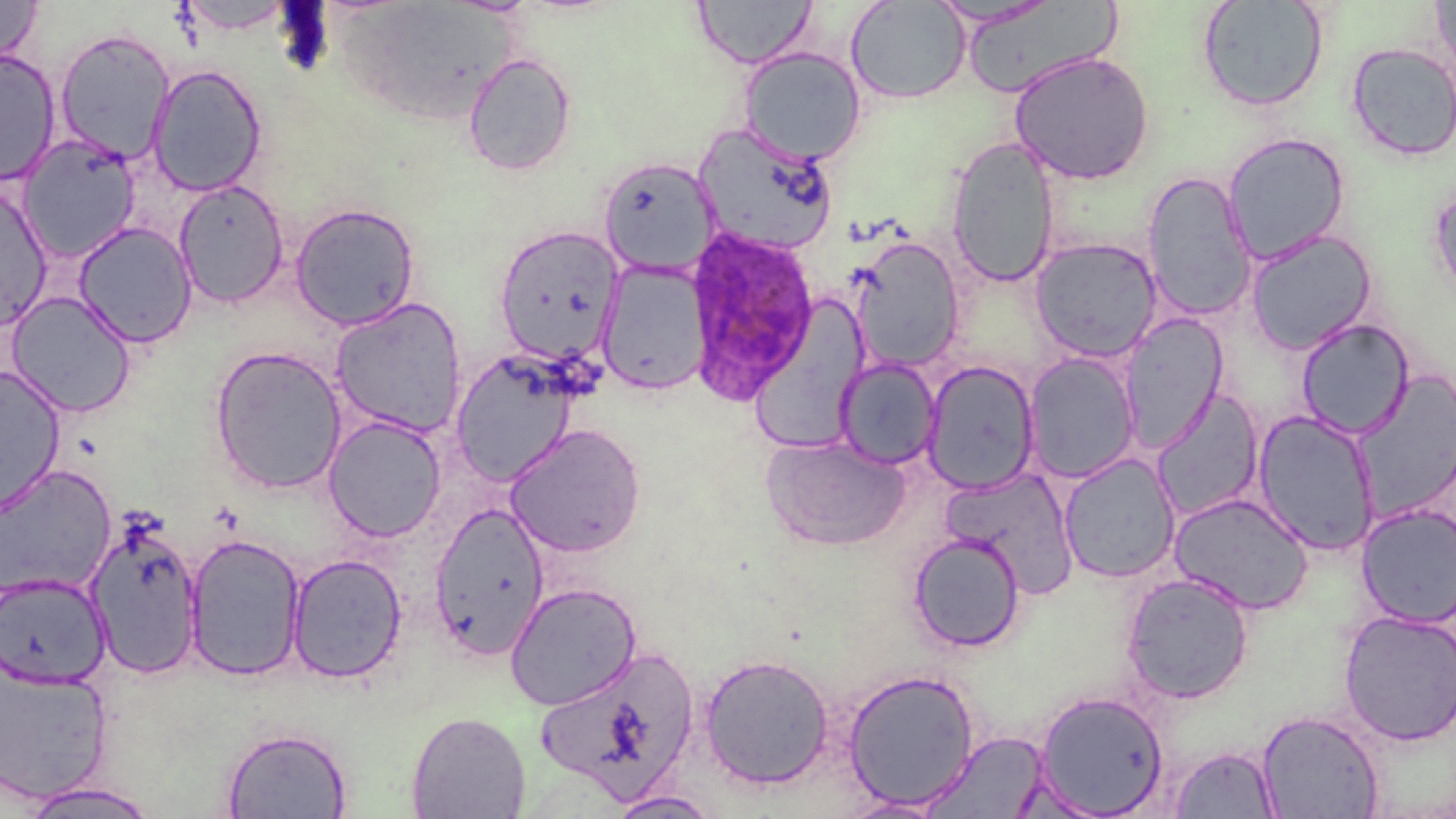

slide-level diagnosis = Plasmodium ovale
preparation = thin blood smear
Plasmodium ovale-infected red blood cell locations = approximate bounding boxes as [x1, y1, x2, y2] in pixels: [683, 225, 819, 404]
image size = 1456×819 pixels
field of view = one of a larger specimen
magnification = 1000x
stain = May-Grünwald-Giemsa
modality = light microscopy
uninfected red blood cell locations = approximate bounding boxes as [x1, y1, x2, y2] in pixels: [693, 0, 816, 68], [1196, 0, 1328, 112], [1430, 0, 1456, 83], [0, 1, 43, 66], [846, 1, 970, 104], [54, 28, 175, 164], [1347, 42, 1456, 161], [738, 47, 866, 165], [0, 50, 61, 186], [1008, 51, 1155, 184], [463, 53, 576, 176], [147, 64, 268, 197], [694, 124, 837, 255], [1222, 132, 1351, 266], [17, 134, 142, 263], [945, 136, 1061, 288], [598, 156, 720, 277], [1141, 170, 1257, 323], [1428, 178, 1456, 303], [173, 179, 289, 309], [0, 183, 54, 332], [290, 202, 421, 330], [73, 221, 197, 348], [493, 226, 624, 366], [1244, 230, 1379, 355], [849, 236, 964, 372], [1030, 236, 1163, 363], [598, 260, 710, 396], [6, 291, 136, 418], [329, 297, 467, 438], [1118, 312, 1228, 452], [1282, 319, 1401, 551], [1296, 319, 1415, 439], [208, 345, 348, 495], [450, 349, 581, 485], [1023, 352, 1141, 484], [835, 358, 941, 469], [922, 360, 1040, 494], [0, 365, 67, 518], [1152, 388, 1264, 521], [1252, 409, 1380, 555], [322, 414, 447, 542], [504, 424, 646, 558], [761, 434, 911, 551], [1059, 452, 1181, 584], [0, 464, 117, 600], [942, 466, 1081, 600], [1167, 491, 1315, 615], [429, 502, 550, 661], [1356, 503, 1456, 627], [85, 518, 204, 679], [184, 532, 306, 681], [907, 532, 1025, 652], [286, 553, 407, 684], [1120, 572, 1255, 704], [0, 574, 111, 689], [505, 582, 642, 710], [1337, 609, 1456, 746], [533, 644, 700, 800], [699, 653, 835, 789], [0, 660, 114, 805], [842, 669, 979, 809], [1034, 689, 1169, 817], [1256, 709, 1385, 819], [406, 710, 531, 819], [221, 725, 353, 819], [922, 732, 1052, 818], [1168, 745, 1280, 818], [14, 782, 162, 818], [607, 790, 721, 818], [839, 797, 948, 818]